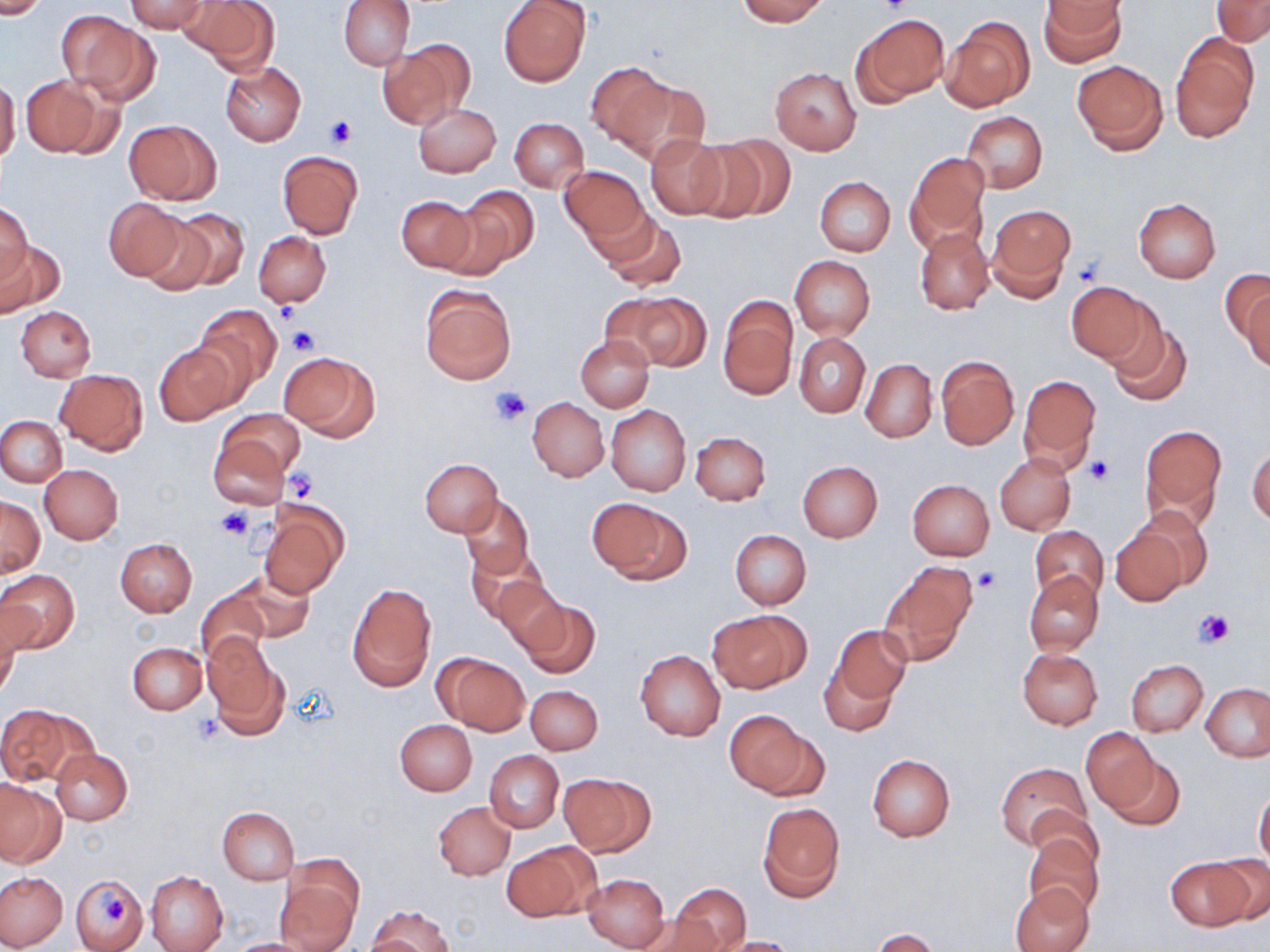
Approximate bounding boxes as [x1, y1, x2, y2] in pixels. Platelet locations: [878, 0, 914, 17], [325, 115, 359, 148], [1070, 255, 1108, 288], [275, 299, 304, 325], [285, 326, 319, 356], [491, 387, 530, 424], [1085, 456, 1113, 486], [282, 471, 317, 502], [217, 507, 252, 541], [972, 567, 1001, 593], [1195, 609, 1234, 648], [192, 713, 224, 744], [100, 889, 132, 923]. Uninfected red blood cell locations: [0, 0, 51, 19], [180, 0, 279, 76], [338, 0, 415, 70], [499, 0, 591, 87], [736, 0, 829, 25], [1040, 0, 1125, 66], [1212, 0, 1270, 45], [123, 1, 208, 33], [59, 12, 159, 104], [856, 14, 947, 105], [943, 18, 1034, 112], [1170, 35, 1259, 142], [377, 40, 471, 128], [1072, 59, 1168, 153], [584, 61, 671, 149], [220, 62, 306, 145], [770, 66, 863, 155], [21, 75, 112, 157], [0, 78, 20, 164], [617, 80, 710, 167], [413, 102, 501, 177], [961, 111, 1048, 194], [509, 118, 588, 192], [125, 119, 221, 205], [645, 133, 730, 219], [690, 136, 784, 224], [278, 150, 363, 238], [905, 152, 991, 250], [559, 165, 648, 246], [814, 177, 895, 256], [451, 185, 539, 273], [396, 195, 476, 273], [103, 198, 188, 282], [1133, 198, 1220, 282], [1, 201, 32, 285], [984, 205, 1075, 301], [163, 209, 250, 292], [599, 213, 686, 292], [140, 216, 217, 294], [914, 228, 994, 314], [254, 231, 330, 307], [0, 240, 65, 316], [7, 245, 79, 380], [789, 255, 875, 339], [1224, 270, 1269, 360], [1068, 280, 1158, 367], [419, 285, 515, 385], [624, 292, 711, 373], [1242, 293, 1270, 372], [719, 298, 797, 398], [195, 305, 280, 393], [15, 306, 96, 381], [1107, 317, 1192, 407], [794, 333, 869, 417], [576, 335, 654, 412], [155, 341, 239, 423], [280, 351, 380, 440], [935, 356, 1018, 449], [861, 358, 937, 442], [55, 369, 148, 454], [1018, 375, 1101, 470], [527, 397, 608, 482], [605, 405, 691, 496], [216, 408, 305, 481], [0, 416, 67, 487], [1139, 425, 1227, 525], [690, 432, 771, 505], [208, 433, 291, 511], [1247, 445, 1270, 525], [995, 453, 1076, 534], [420, 459, 503, 536], [796, 461, 882, 542], [40, 465, 123, 543], [906, 479, 994, 560], [1, 495, 45, 575], [460, 496, 535, 578], [588, 498, 690, 583], [259, 499, 347, 597], [1127, 504, 1217, 592], [1108, 522, 1191, 608], [1029, 526, 1108, 602], [730, 530, 811, 609], [115, 538, 197, 617], [465, 545, 547, 624], [885, 561, 977, 657], [0, 569, 79, 652], [234, 570, 314, 641], [1024, 570, 1104, 657], [488, 573, 568, 654], [347, 581, 437, 690], [195, 589, 270, 666], [519, 598, 599, 677], [707, 609, 810, 690], [0, 611, 22, 700], [832, 625, 912, 707], [201, 637, 286, 734], [128, 641, 207, 715], [635, 650, 726, 740], [1017, 650, 1102, 729], [434, 652, 530, 735], [820, 656, 900, 737], [1126, 659, 1208, 736], [1202, 683, 1269, 760], [526, 684, 602, 754], [3, 703, 97, 788], [724, 709, 818, 798], [394, 719, 477, 795], [1084, 727, 1159, 813], [51, 748, 133, 825], [1102, 749, 1185, 831], [484, 751, 564, 832], [867, 754, 955, 841], [995, 762, 1091, 850], [559, 772, 654, 856], [0, 778, 64, 867], [1254, 787, 1270, 867], [434, 801, 514, 880], [758, 803, 844, 901], [218, 807, 298, 884], [1022, 828, 1105, 915], [502, 842, 598, 923], [1210, 853, 1270, 926], [1166, 856, 1253, 929], [0, 871, 67, 949], [146, 871, 228, 952], [71, 872, 148, 952], [582, 872, 670, 950], [274, 873, 360, 952], [1013, 882, 1091, 952], [670, 884, 750, 951], [365, 904, 455, 952], [637, 911, 722, 952], [872, 929, 943, 952], [713, 936, 800, 951], [222, 938, 320, 952]. Slide-level diagnosis: no evidence of blood parasites. May-Grünwald-Giemsa stain. Thin blood film. One field of a larger specimen. 1000x magnification. Optical microscopy. Image is 1270×952 pixels.